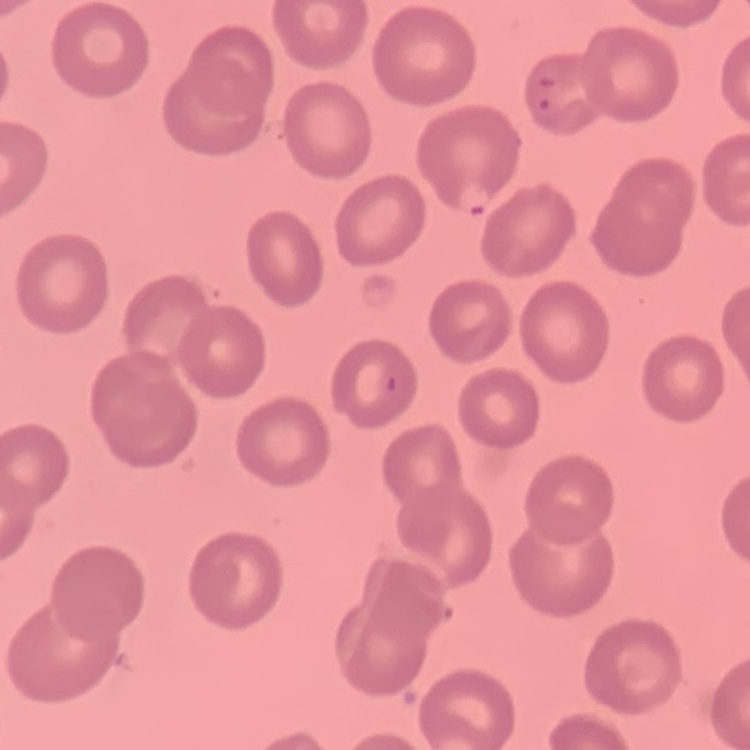

The erythrocytes show no rouleaux formation. Thin peripheral smear. Stained with either Field's or Giemsa. One tile cut from a larger photomicrograph.